Point out every malaria parasite and every leukocyte.
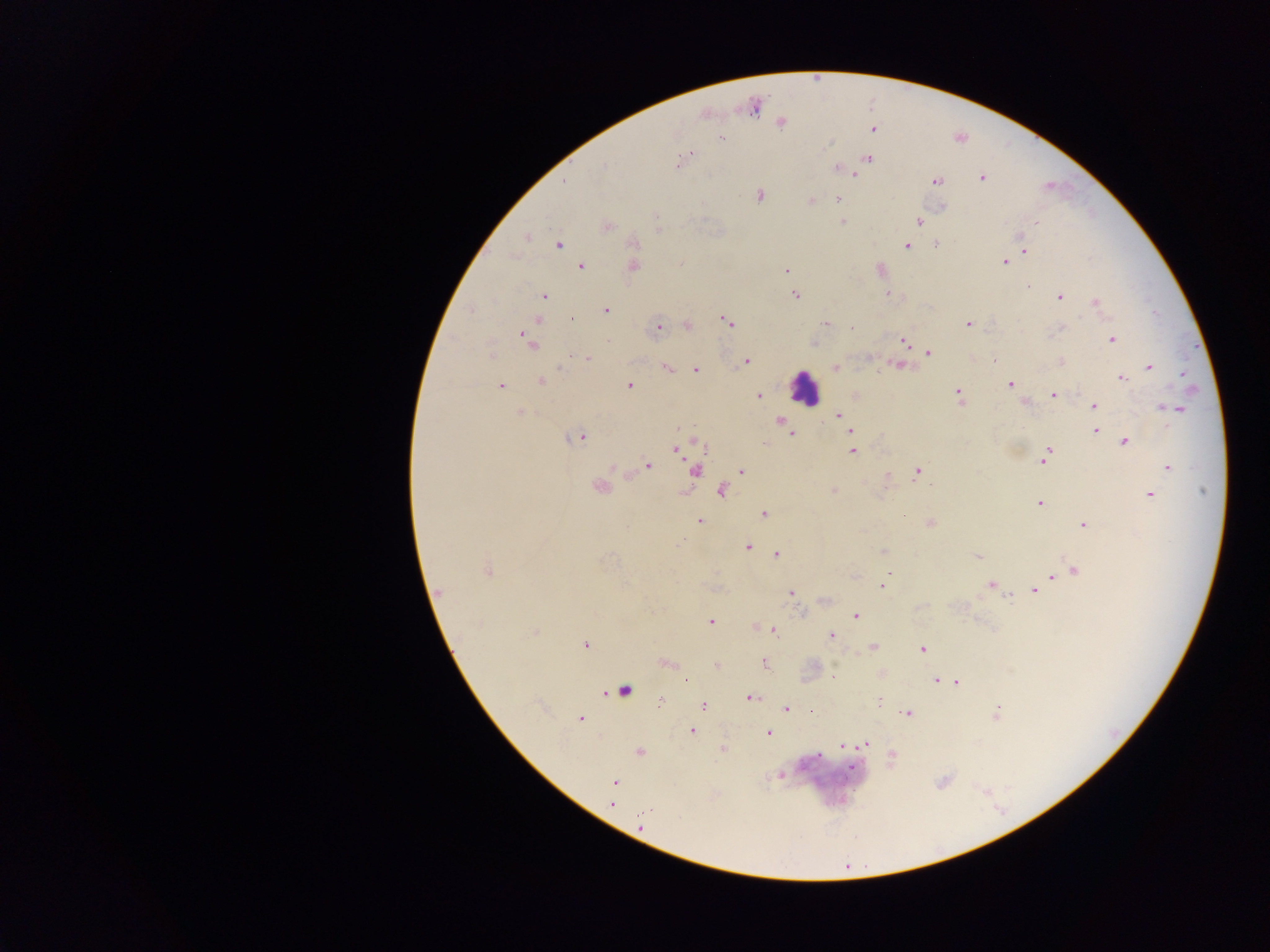
Approximate centers as (x, y) in pixels.
Malaria parasites: (753, 108), (781, 123), (873, 129), (722, 138), (689, 154), (685, 157), (869, 158), (678, 162), (604, 167), (836, 169), (855, 174), (981, 178), (564, 181), (936, 181), (760, 195), (838, 199), (812, 200), (656, 216), (843, 222), (918, 222), (1037, 223), (607, 226), (527, 238), (634, 243), (558, 244), (936, 244), (906, 246), (1025, 251), (1004, 262), (680, 264), (634, 266), (581, 267), (786, 270), (1028, 286), (794, 294), (888, 294), (543, 296), (1060, 297), (1095, 302), (605, 310), (572, 319), (727, 322), (826, 323), (968, 324), (687, 325), (659, 326), (851, 327), (1061, 328), (528, 337), (1112, 340), (904, 341), (928, 353), (491, 354), (587, 357), (994, 360), (1061, 361), (747, 362), (899, 365), (1149, 366), (836, 367), (667, 368), (696, 369), (1183, 374), (1121, 379), (542, 381), (1010, 384), (500, 386), (629, 386), (958, 395), (1054, 395), (758, 396), (1094, 406), (1176, 409), (519, 413), (838, 415), (781, 421), (1095, 431), (852, 432), (792, 434), (577, 438), (1125, 442), (763, 443), (676, 450), (853, 451), (1045, 459), (648, 466), (1168, 467), (613, 468), (742, 471), (917, 471), (695, 472), (931, 486), (599, 488), (721, 491), (834, 491), (1149, 495), (1040, 504), (764, 514), (700, 521), (930, 524), (1083, 525), (747, 547), (884, 552), (777, 554), (978, 556), (487, 570), (1075, 571), (1052, 575), (990, 585), (883, 586), (1036, 590), (440, 592), (791, 593), (1010, 598), (855, 616), (710, 621), (755, 627), (774, 630), (535, 632), (831, 635), (585, 645), (873, 647), (922, 649), (765, 663), (666, 664), (716, 666), (833, 676), (936, 681), (957, 682), (624, 689), (750, 698), (879, 699), (660, 702), (703, 706), (786, 708), (812, 711), (996, 712), (906, 713), (579, 718), (692, 730), (768, 733), (867, 743), (842, 745), (723, 748), (639, 752), (892, 755), (852, 767), (615, 782), (613, 802).
Leukocytes: (804, 387).

Summary:
  - Preparation: thick blood film
  - Capture: mobile-phone photograph through a microscope
  - Country: Ghana
  - Image size: 1270×952 pixels
  - Field of view: single